Report the malaria status of this cell.
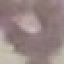

It is uninfected.

{
  "stain": "Giemsa",
  "image_type": "automatically extracted cell patch, resized to 64 × 64 pixels",
  "capture": "smartphone camera at the microscope eyepiece",
  "preparation": "thin blood film"
}